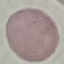

Malaria status: uninfected. Giemsa-stained preparation. Automatically extracted cell patch, resized to 64 × 64 pixels. Acquired by smartphone through the microscope eyepiece. Thin blood smear.